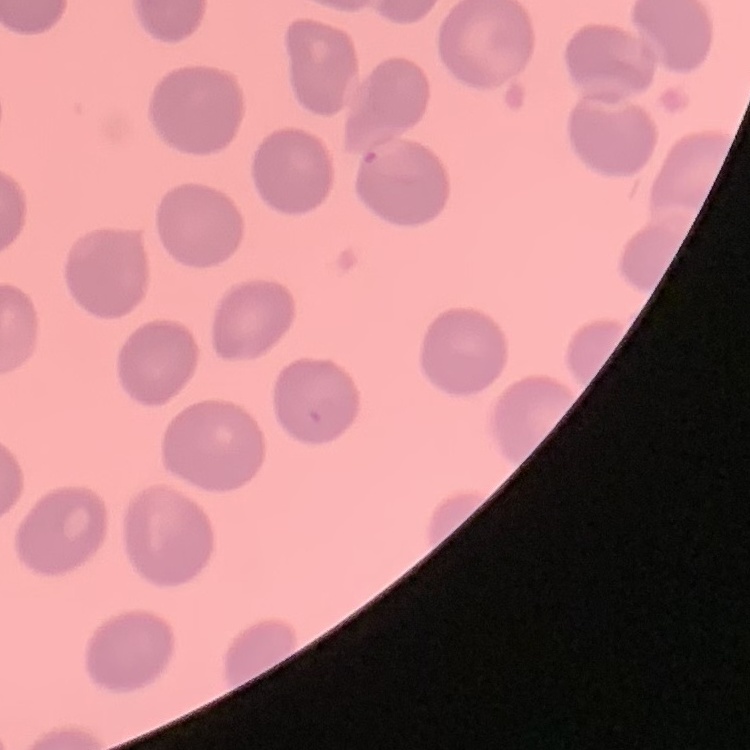

{
  "erythrocyte_morphology": "no rouleaux formation",
  "image_type": "square crop of a larger photomicrograph",
  "preparation": "thin peripheral smear",
  "stain": "Field's or Giemsa"
}